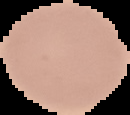
result = no Plasmodium parasites detected
image type = segmented cell region with the area outside set to black
preparation = thin blood smear
image size = 130×115 pixels